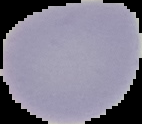
Summary:
  - Image type: segmented cell region with the area outside set to black
  - Malaria status: uninfected
  - Image size: 142×124 pixels
  - Preparation: thin blood smear